Locate and identify every blood parasite.
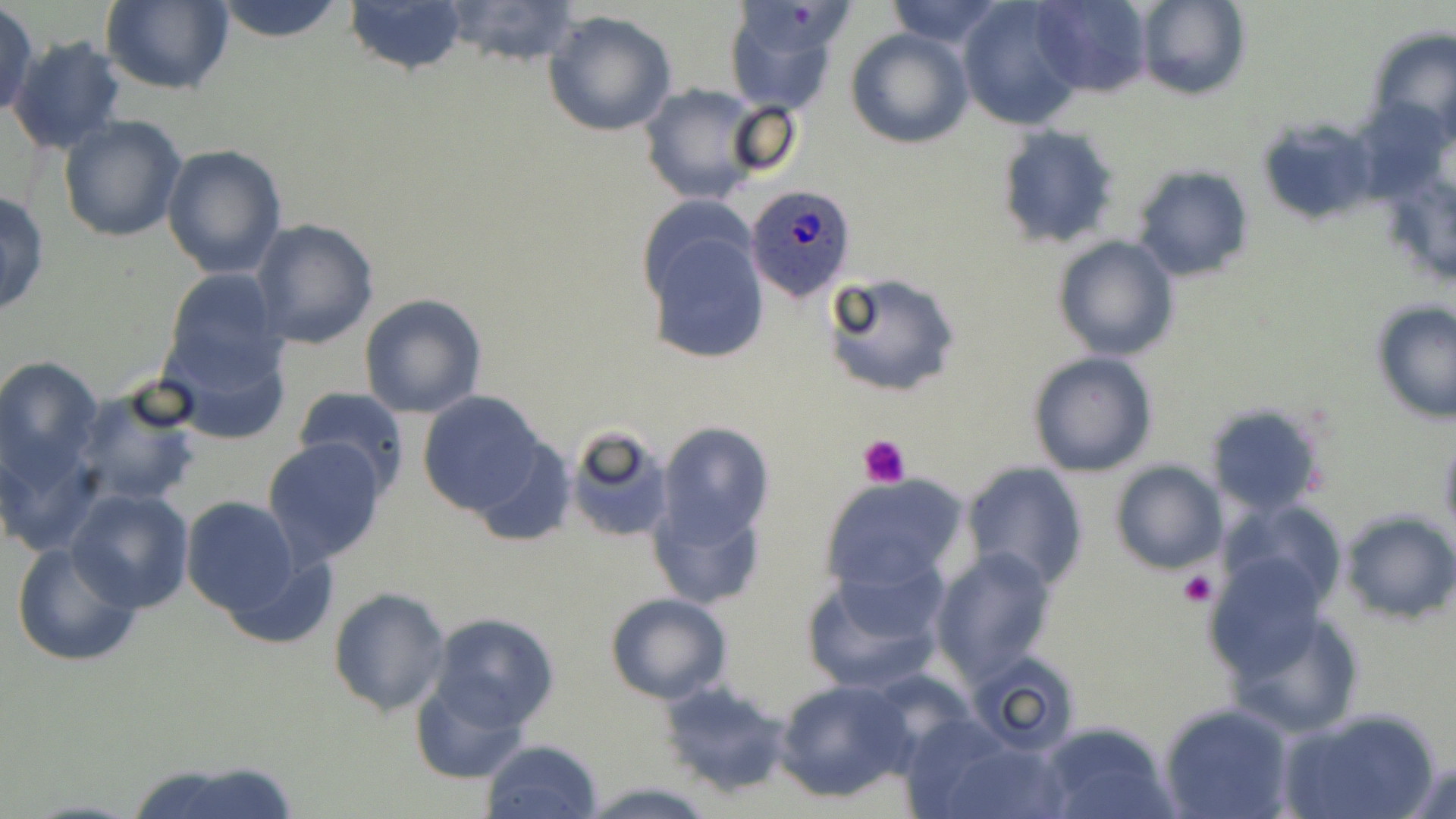
Approximate bounding boxes as named x1/y1/x2/y2 corners in pixels.
Plasmodium ovale-infected red blood cells: (x1=745, y1=182, x2=857, y2=300).
No Plasmodium falciparum, Plasmodium malariae, Plasmodium vivax, Babesia divergens, or Trypanosoma brucei observed.

Summary:
  - Platelet locations: (x1=858, y1=435, x2=911, y2=488), (x1=1178, y1=570, x2=1216, y2=607)
  - Uninfected red blood cell locations: (x1=436, y1=0, x2=584, y2=71), (x1=884, y1=0, x2=1009, y2=48), (x1=956, y1=0, x2=1089, y2=130), (x1=1030, y1=0, x2=1154, y2=97), (x1=100, y1=1, x2=234, y2=94), (x1=209, y1=1, x2=351, y2=44), (x1=343, y1=1, x2=470, y2=76), (x1=1134, y1=1, x2=1250, y2=101), (x1=724, y1=2, x2=850, y2=113), (x1=1, y1=3, x2=38, y2=118), (x1=542, y1=9, x2=679, y2=138), (x1=1365, y1=26, x2=1456, y2=147), (x1=846, y1=28, x2=973, y2=149), (x1=7, y1=36, x2=126, y2=155), (x1=637, y1=83, x2=766, y2=204), (x1=725, y1=102, x2=804, y2=181), (x1=58, y1=114, x2=187, y2=243), (x1=993, y1=124, x2=1121, y2=252), (x1=162, y1=145, x2=287, y2=280), (x1=1130, y1=165, x2=1254, y2=282), (x1=0, y1=190, x2=50, y2=319), (x1=251, y1=219, x2=380, y2=351), (x1=640, y1=222, x2=770, y2=367), (x1=1052, y1=235, x2=1180, y2=362), (x1=161, y1=268, x2=287, y2=389), (x1=824, y1=271, x2=962, y2=398), (x1=359, y1=293, x2=488, y2=419), (x1=1371, y1=302, x2=1456, y2=423), (x1=160, y1=331, x2=295, y2=444), (x1=1028, y1=351, x2=1158, y2=478), (x1=0, y1=356, x2=102, y2=484), (x1=72, y1=385, x2=203, y2=509), (x1=293, y1=387, x2=409, y2=497), (x1=418, y1=391, x2=546, y2=519), (x1=1203, y1=402, x2=1327, y2=515), (x1=656, y1=422, x2=774, y2=549), (x1=564, y1=426, x2=674, y2=543), (x1=1438, y1=432, x2=1456, y2=540), (x1=0, y1=435, x2=100, y2=555), (x1=472, y1=437, x2=574, y2=548), (x1=262, y1=438, x2=387, y2=566), (x1=1108, y1=459, x2=1227, y2=575), (x1=962, y1=461, x2=1088, y2=590), (x1=819, y1=475, x2=971, y2=599), (x1=649, y1=481, x2=768, y2=612), (x1=66, y1=487, x2=195, y2=613), (x1=181, y1=496, x2=303, y2=618), (x1=1225, y1=499, x2=1349, y2=612), (x1=1338, y1=510, x2=1455, y2=624), (x1=10, y1=539, x2=143, y2=668), (x1=930, y1=548, x2=1058, y2=684), (x1=220, y1=550, x2=337, y2=653), (x1=1204, y1=555, x2=1329, y2=685), (x1=803, y1=564, x2=946, y2=693), (x1=328, y1=588, x2=452, y2=715), (x1=605, y1=592, x2=733, y2=704), (x1=1223, y1=598, x2=1367, y2=741), (x1=426, y1=613, x2=558, y2=736), (x1=967, y1=650, x2=1085, y2=755), (x1=655, y1=677, x2=794, y2=800), (x1=774, y1=678, x2=915, y2=803), (x1=411, y1=680, x2=530, y2=784), (x1=1158, y1=701, x2=1296, y2=819), (x1=1280, y1=707, x2=1437, y2=819), (x1=1037, y1=721, x2=1179, y2=819), (x1=926, y1=735, x2=1073, y2=819), (x1=480, y1=739, x2=604, y2=819), (x1=1403, y1=757, x2=1456, y2=818), (x1=124, y1=759, x2=302, y2=819), (x1=585, y1=781, x2=716, y2=818)
  - Slide-level diagnosis: Plasmodium ovale
  - Image size: 1456×819 pixels
  - Stain: May-Grünwald-Giemsa
  - Magnification: 1000x
  - Field of view: single
  - Preparation: thin blood film
  - Modality: light microscopy